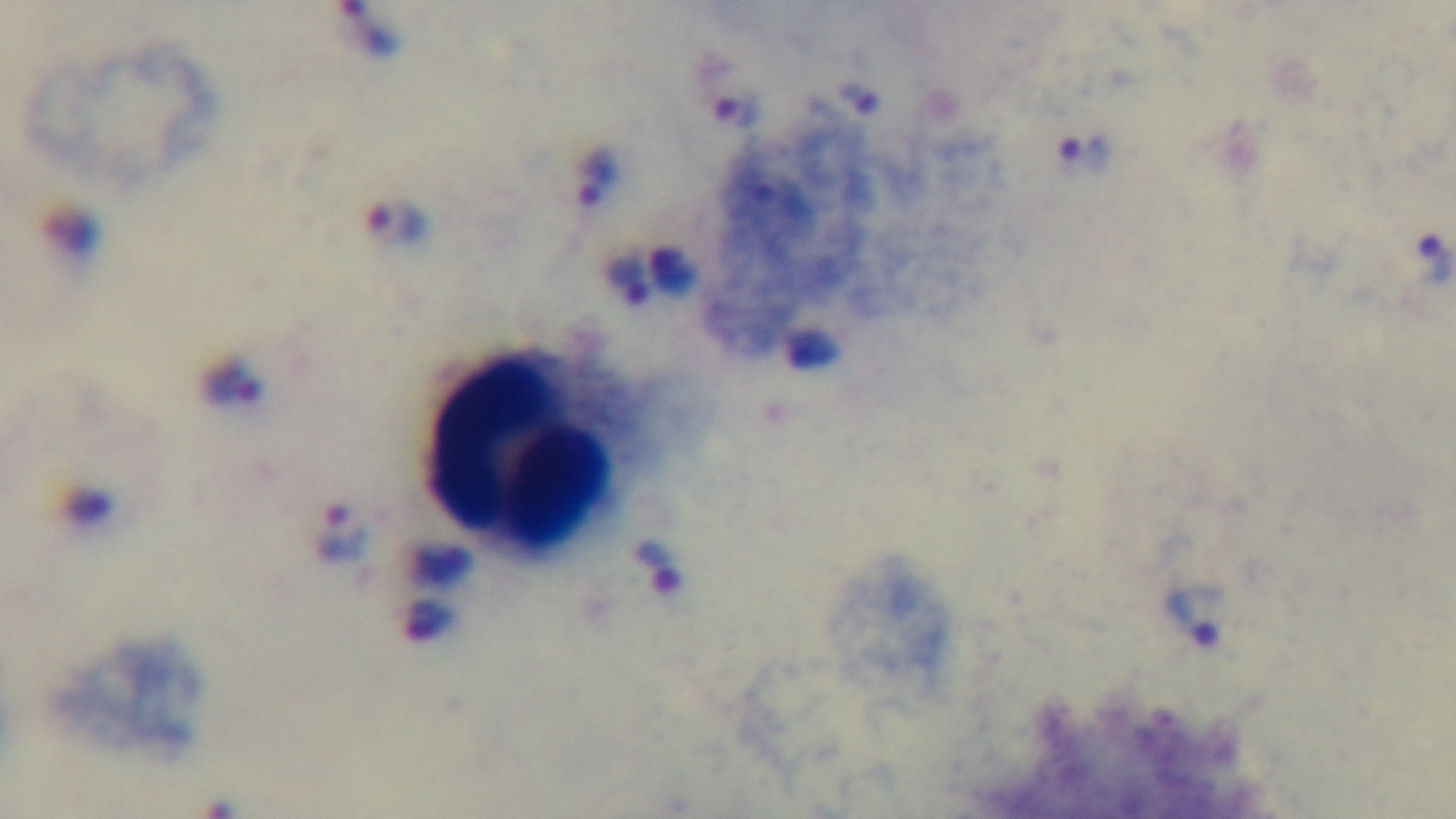
modality: light microscopy
stain: Giemsa
objective: 100x oil immersion
preparation: thick
malaria_status: positive
field_of_view: single
capture: mounted 4K digital camera